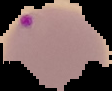

From a thin blood smear. Image is 112×91 pixels. The area outside the segmented cell region is set to black. Malaria status: parasitized.